Give the extent of all Plasmodium falciparum-infected red blood cells.
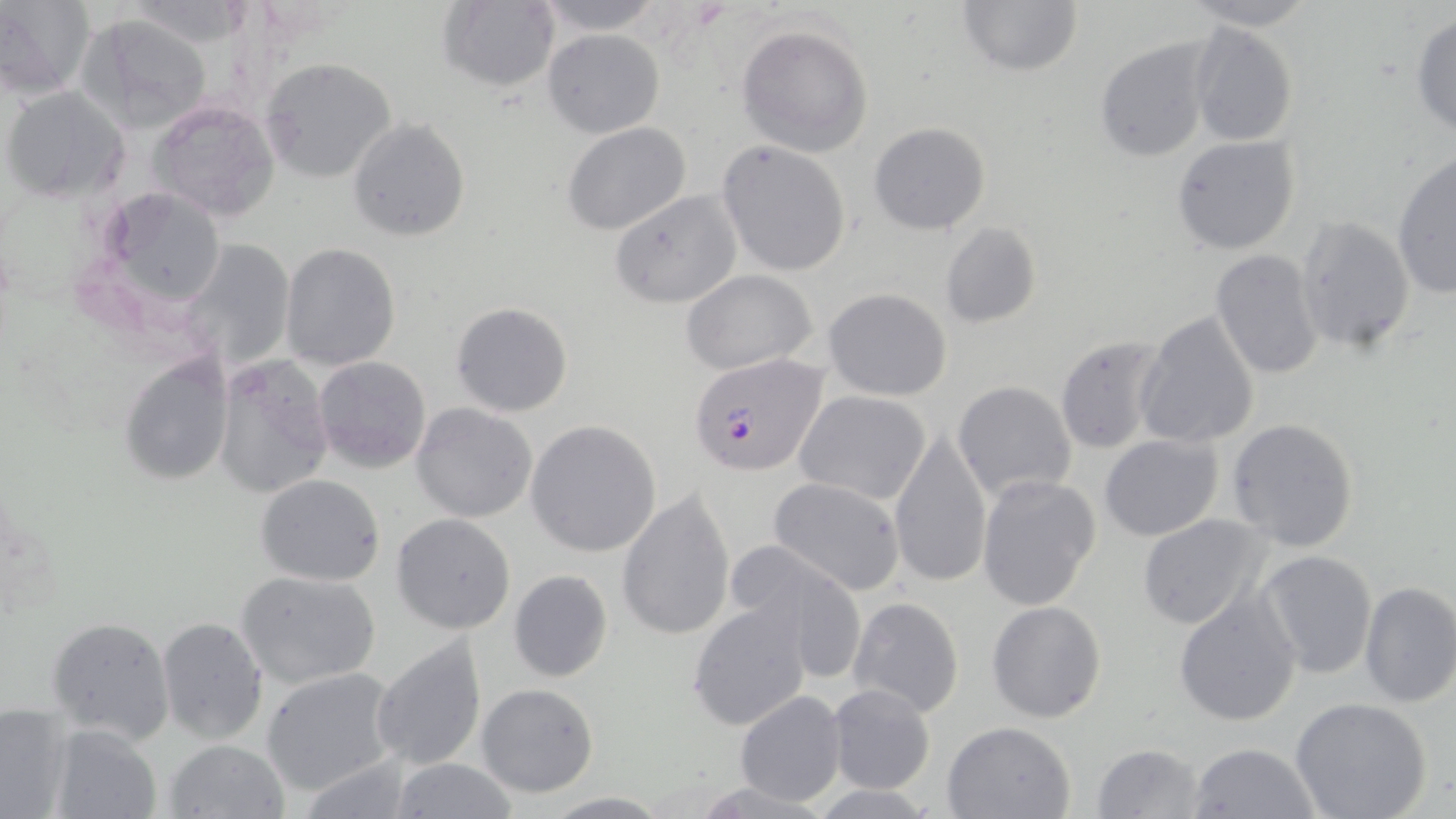
Approximate bounding boxes as named x1/y1/x2/y2 corners in pixels.
Plasmodium falciparum-infected red blood cells: (x1=689, y1=354, x2=826, y2=476).

Uninfected red blood cell locations: (x1=1, y1=0, x2=94, y2=98), (x1=115, y1=0, x2=256, y2=48), (x1=533, y1=0, x2=665, y2=34), (x1=956, y1=0, x2=1084, y2=75), (x1=1182, y1=0, x2=1318, y2=29), (x1=436, y1=1, x2=561, y2=92), (x1=1410, y1=11, x2=1456, y2=137), (x1=78, y1=13, x2=217, y2=132), (x1=1189, y1=18, x2=1299, y2=148), (x1=734, y1=22, x2=876, y2=157), (x1=542, y1=28, x2=664, y2=137), (x1=1096, y1=38, x2=1213, y2=163), (x1=259, y1=57, x2=397, y2=183), (x1=2, y1=87, x2=130, y2=203), (x1=146, y1=98, x2=282, y2=225), (x1=348, y1=118, x2=470, y2=240), (x1=562, y1=122, x2=692, y2=235), (x1=868, y1=123, x2=992, y2=235), (x1=1172, y1=135, x2=1301, y2=256), (x1=717, y1=140, x2=851, y2=276), (x1=1391, y1=153, x2=1456, y2=299), (x1=97, y1=187, x2=229, y2=311), (x1=608, y1=190, x2=743, y2=309), (x1=1294, y1=215, x2=1417, y2=354), (x1=940, y1=221, x2=1041, y2=329), (x1=185, y1=238, x2=298, y2=372), (x1=279, y1=242, x2=401, y2=370), (x1=1210, y1=250, x2=1325, y2=378), (x1=681, y1=269, x2=818, y2=374), (x1=823, y1=287, x2=952, y2=401), (x1=452, y1=302, x2=573, y2=417), (x1=1134, y1=311, x2=1260, y2=450), (x1=1055, y1=335, x2=1168, y2=454), (x1=117, y1=353, x2=236, y2=488), (x1=212, y1=356, x2=334, y2=499), (x1=314, y1=356, x2=432, y2=472), (x1=951, y1=380, x2=1078, y2=502), (x1=793, y1=390, x2=932, y2=505), (x1=411, y1=402, x2=538, y2=523), (x1=1227, y1=417, x2=1361, y2=552), (x1=525, y1=419, x2=661, y2=558), (x1=888, y1=429, x2=994, y2=588), (x1=1099, y1=432, x2=1224, y2=541), (x1=255, y1=475, x2=385, y2=587), (x1=976, y1=475, x2=1103, y2=613), (x1=769, y1=477, x2=906, y2=596), (x1=618, y1=490, x2=736, y2=641), (x1=1136, y1=512, x2=1270, y2=630), (x1=392, y1=513, x2=516, y2=635), (x1=725, y1=542, x2=867, y2=679), (x1=1257, y1=551, x2=1377, y2=679), (x1=508, y1=569, x2=613, y2=682), (x1=235, y1=570, x2=381, y2=689), (x1=1357, y1=580, x2=1456, y2=709), (x1=1174, y1=589, x2=1302, y2=726), (x1=847, y1=596, x2=964, y2=720), (x1=687, y1=599, x2=814, y2=731), (x1=986, y1=599, x2=1107, y2=723), (x1=46, y1=615, x2=176, y2=745), (x1=156, y1=617, x2=268, y2=745), (x1=372, y1=634, x2=487, y2=773), (x1=261, y1=668, x2=403, y2=795), (x1=475, y1=682, x2=600, y2=798), (x1=826, y1=683, x2=937, y2=797), (x1=735, y1=691, x2=847, y2=805), (x1=1289, y1=696, x2=1433, y2=819), (x1=0, y1=703, x2=75, y2=818), (x1=942, y1=719, x2=1077, y2=818), (x1=45, y1=722, x2=162, y2=819), (x1=163, y1=738, x2=291, y2=819), (x1=1092, y1=743, x2=1205, y2=819), (x1=1190, y1=743, x2=1321, y2=819), (x1=391, y1=757, x2=517, y2=819), (x1=545, y1=792, x2=670, y2=817). Slide-level diagnosis: Plasmodium falciparum. Single field of view. May-Grünwald-Giemsa-stained preparation. Image is 1456×819 pixels. Thin blood film. Optical microscopy. 1000x magnification.